Locate every blood parasite and identify its species.
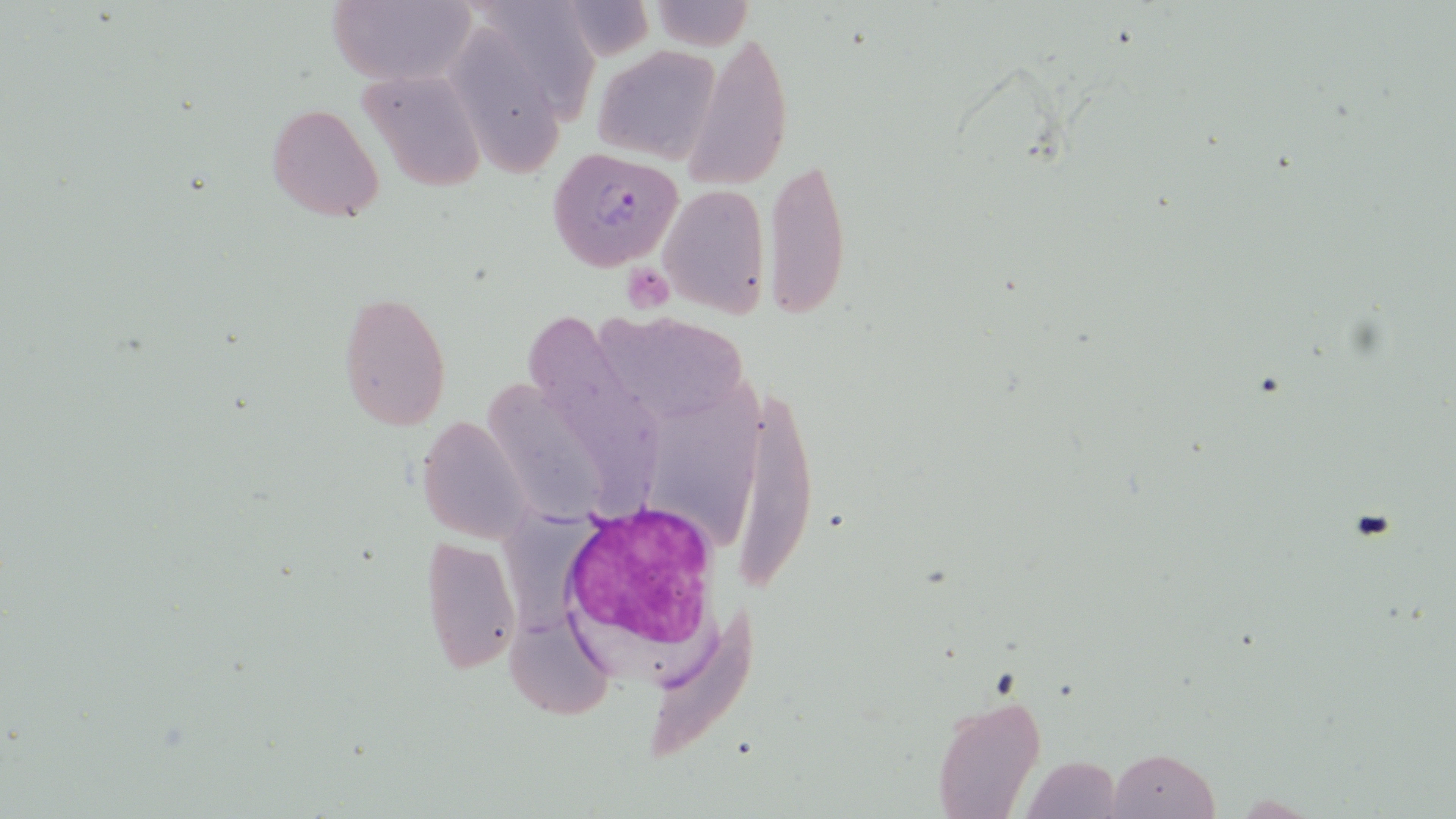
Approximate bounding boxes as (x1, y1, x2, y2) in pixels.
Plasmodium falciparum-infected red blood cells: (548, 146, 684, 271).
No Plasmodium ovale, Plasmodium malariae, Plasmodium vivax, Babesia divergens, or Trypanosoma brucei observed.

Summary:
  - White blood cell locations: (556, 499, 721, 666)
  - Uninfected red blood cell locations: (323, 0, 478, 85), (476, 0, 597, 125), (648, 2, 757, 48), (453, 23, 563, 176), (685, 24, 793, 190), (593, 41, 723, 165), (356, 69, 490, 193), (267, 102, 384, 222), (765, 152, 853, 318), (659, 181, 769, 318), (336, 290, 452, 430), (525, 306, 652, 499), (590, 316, 755, 417), (487, 366, 626, 516), (652, 378, 780, 532), (736, 389, 823, 601), (416, 414, 535, 544), (492, 495, 578, 630), (419, 533, 522, 676), (639, 602, 762, 769), (507, 614, 614, 722), (931, 691, 1046, 818), (1022, 735, 1129, 819), (1108, 749, 1221, 819)
  - Platelet locations: (625, 269, 670, 320)
  - Slide-level diagnosis: Plasmodium falciparum
  - Preparation: thin blood smear
  - Field of view: one of a larger specimen
  - Modality: optical microscopy
  - Image size: 1456×819 pixels
  - Magnification: 1000x
  - Stain: May-Grünwald-Giemsa